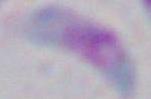
identification: Toxoplasma gondii
magnification: 1000x
modality: micrograph